Point out cells.
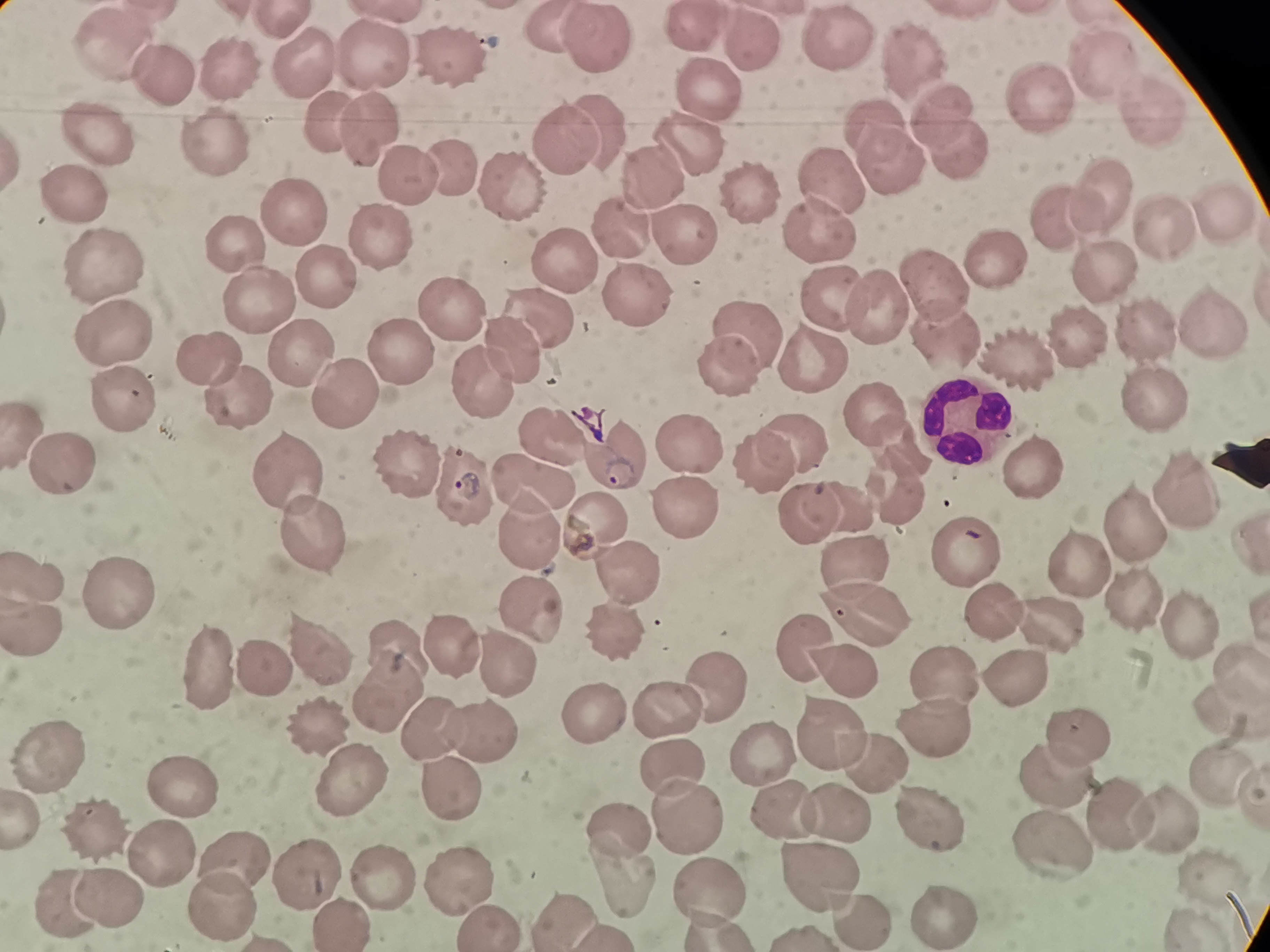
Approximate centers as [x, y] in pixels.
Cells: [685, 31], [598, 40], [834, 44], [114, 46], [753, 48], [906, 53], [378, 57], [457, 58], [1100, 67], [302, 69], [228, 70], [170, 74], [706, 100], [1033, 104], [1146, 109], [943, 114], [328, 118], [873, 126], [96, 131], [372, 132], [602, 134], [558, 136], [208, 143], [694, 146], [953, 153], [456, 166], [886, 172], [406, 180], [649, 181], [515, 184], [1105, 185], [746, 188], [833, 188], [78, 192], [1219, 208], [294, 215], [1060, 217], [1160, 223], [379, 228], [620, 231], [813, 231], [239, 239], [677, 240], [992, 253], [101, 257], [566, 262], [1097, 268], [322, 277], [932, 278], [637, 296], [834, 299], [255, 302], [451, 302], [886, 304], [745, 319], [539, 321], [1216, 321], [1139, 331], [108, 332], [1072, 332], [942, 333], [507, 345], [816, 352], [301, 354], [396, 355], [1017, 359], [210, 360], [730, 364], [482, 378], [1150, 392], [237, 393], [123, 398], [339, 400], [871, 407], [965, 416], [542, 433], [894, 437], [792, 438], [689, 446], [757, 459], [405, 460], [612, 461], [61, 466], [1033, 466], [463, 477], [284, 480], [535, 482], [1185, 489], [846, 503], [681, 508], [805, 515], [1132, 522], [592, 525], [535, 532], [315, 538], [965, 551], [1075, 561], [845, 565], [624, 570], [35, 575], [124, 596], [1141, 601], [537, 604], [867, 607], [989, 609], [1047, 619], [1187, 625], [35, 629], [614, 635], [811, 641], [394, 646], [455, 647], [318, 653], [505, 654], [264, 666], [843, 668], [1236, 670], [213, 672], [1008, 675], [945, 679], [715, 682], [387, 688], [1224, 703], [664, 710], [591, 712], [437, 723], [322, 724], [935, 725], [480, 728], [829, 732], [1074, 732], [762, 751], [866, 753], [53, 754], [675, 766], [1219, 771], [356, 775], [186, 780], [1048, 780], [453, 782], [781, 804], [837, 807], [683, 813], [927, 815], [1110, 816], [1154, 816], [621, 821], [96, 825], [1045, 839], [236, 849], [165, 851], [304, 864], [816, 867], [378, 870], [617, 871], [451, 874], [1211, 878], [708, 882], [103, 891], [63, 897], [217, 899], [943, 913], [568, 915], [854, 915], [336, 917], [483, 917].

Giemsa-stained preparation. Thin smear of blood. Acquired by smartphone through the microscope eyepiece. Single field of view. Image is 1270×952 pixels.